Classify this cell by malaria status.
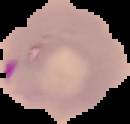
Parasitized.

Cell region segmented out of the field of view; the surrounding area is masked to black. Image is 130×124 pixels. From a thin blood smear.